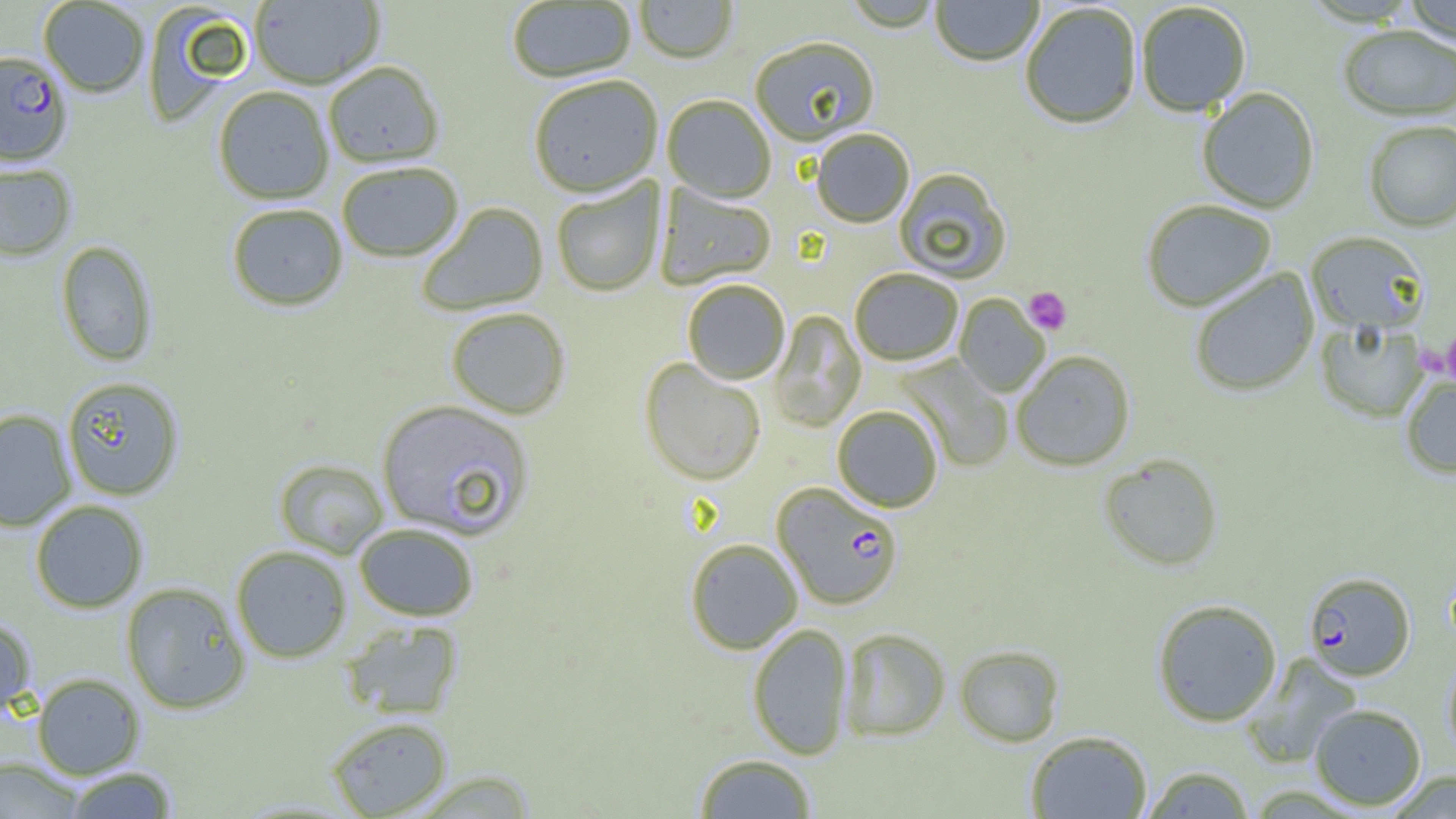

Summary:
  - Coordinate format: approximate bounding boxes as named x1/y1/x2/y2 corners in pixels
  - Uninfected red blood cell locations: (x1=249, y1=0, x2=385, y2=89), (x1=633, y1=0, x2=737, y2=64), (x1=930, y1=0, x2=1043, y2=67), (x1=1401, y1=0, x2=1456, y2=47), (x1=38, y1=1, x2=150, y2=97), (x1=506, y1=1, x2=636, y2=84), (x1=841, y1=1, x2=945, y2=33), (x1=1020, y1=2, x2=1143, y2=129), (x1=1135, y1=2, x2=1252, y2=117), (x1=142, y1=3, x2=253, y2=125), (x1=1338, y1=25, x2=1456, y2=121), (x1=749, y1=37, x2=880, y2=146), (x1=323, y1=62, x2=444, y2=168), (x1=528, y1=75, x2=663, y2=198), (x1=213, y1=86, x2=334, y2=204), (x1=1196, y1=87, x2=1320, y2=213), (x1=662, y1=95, x2=776, y2=202), (x1=1363, y1=120, x2=1456, y2=231), (x1=811, y1=129, x2=914, y2=228), (x1=337, y1=162, x2=464, y2=262), (x1=0, y1=163, x2=76, y2=261), (x1=894, y1=168, x2=1012, y2=284), (x1=551, y1=178, x2=665, y2=297), (x1=654, y1=184, x2=777, y2=290), (x1=1140, y1=199, x2=1277, y2=311), (x1=417, y1=202, x2=549, y2=317), (x1=227, y1=203, x2=349, y2=312), (x1=1306, y1=230, x2=1431, y2=335), (x1=55, y1=240, x2=158, y2=367), (x1=850, y1=268, x2=963, y2=365), (x1=1189, y1=268, x2=1319, y2=397), (x1=682, y1=278, x2=790, y2=384), (x1=954, y1=293, x2=1049, y2=397), (x1=445, y1=307, x2=571, y2=420), (x1=769, y1=310, x2=866, y2=431), (x1=1316, y1=320, x2=1430, y2=422), (x1=1011, y1=350, x2=1135, y2=470), (x1=895, y1=355, x2=1013, y2=471), (x1=639, y1=358, x2=766, y2=486), (x1=1400, y1=372, x2=1456, y2=479), (x1=61, y1=376, x2=184, y2=500), (x1=376, y1=399, x2=535, y2=542), (x1=832, y1=405, x2=943, y2=512), (x1=0, y1=409, x2=77, y2=531), (x1=1098, y1=453, x2=1223, y2=571), (x1=274, y1=459, x2=388, y2=558), (x1=30, y1=500, x2=148, y2=613), (x1=354, y1=523, x2=479, y2=621), (x1=685, y1=538, x2=803, y2=654), (x1=231, y1=545, x2=352, y2=663), (x1=120, y1=581, x2=251, y2=714), (x1=1152, y1=598, x2=1282, y2=726), (x1=0, y1=615, x2=36, y2=722), (x1=341, y1=620, x2=463, y2=720), (x1=747, y1=623, x2=853, y2=760), (x1=840, y1=627, x2=950, y2=741), (x1=954, y1=644, x2=1064, y2=746), (x1=1242, y1=654, x2=1362, y2=768), (x1=1443, y1=654, x2=1456, y2=764), (x1=31, y1=673, x2=145, y2=779), (x1=1309, y1=703, x2=1427, y2=810), (x1=325, y1=716, x2=452, y2=818), (x1=1025, y1=730, x2=1152, y2=819), (x1=693, y1=753, x2=818, y2=818), (x1=0, y1=758, x2=84, y2=818), (x1=1141, y1=765, x2=1255, y2=818), (x1=64, y1=766, x2=180, y2=818), (x1=407, y1=770, x2=538, y2=818), (x1=1384, y1=770, x2=1456, y2=818)
  - Plasmodium falciparum-infected red blood cell locations: (x1=0, y1=50, x2=72, y2=166), (x1=772, y1=481, x2=903, y2=610), (x1=1303, y1=571, x2=1415, y2=681)
  - Platelet locations: (x1=1023, y1=286, x2=1072, y2=334), (x1=1442, y1=334, x2=1456, y2=382), (x1=1414, y1=340, x2=1451, y2=378)
  - Slide-level diagnosis: Plasmodium falciparum
  - Field of view: single
  - Modality: light microscopy
  - Magnification: 1000x
  - Image size: 1456×819 pixels
  - Preparation: thin blood film